Identify the parasite.
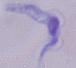
A trypanosome.

Summary:
  - Magnification: 1000x
  - Modality: micrograph